Assess the morphology of the red blood cells.
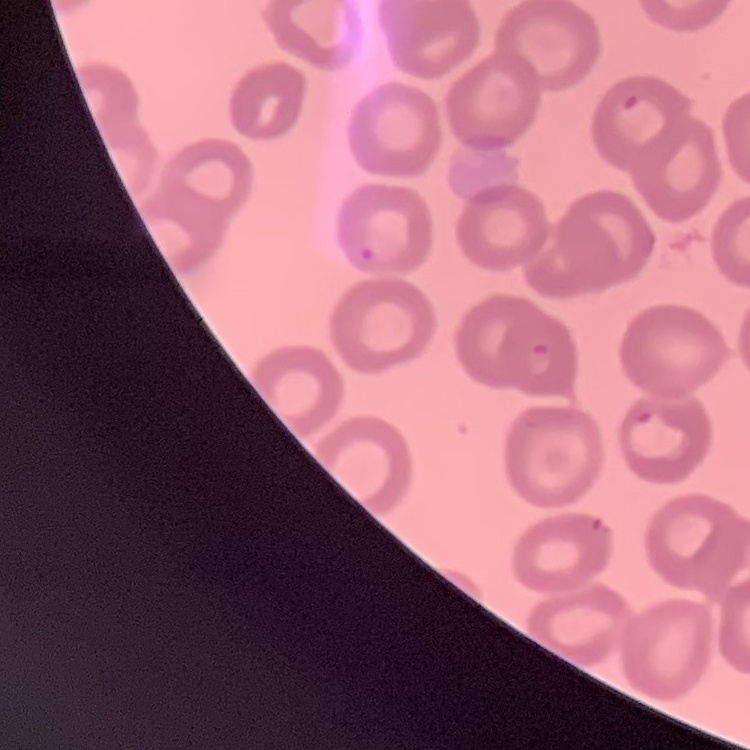

No rouleaux formation.

Summary:
  - Image type: one tile cut from a larger photomicrograph
  - Stain: Field's or Giemsa
  - Preparation: thin blood smear